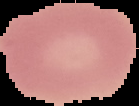
Summary:
  - Result: negative for malaria parasites
  - Image size: 139×106 pixels
  - Preparation: thin blood smear
  - Image type: segmented cell region on a black background